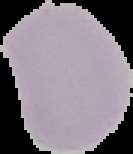

Image is 133×154 pixels. Segmented cell region on a black background. Result: no Plasmodium parasites seen. From a thin blood film.